Find each parasitized red blood cell.
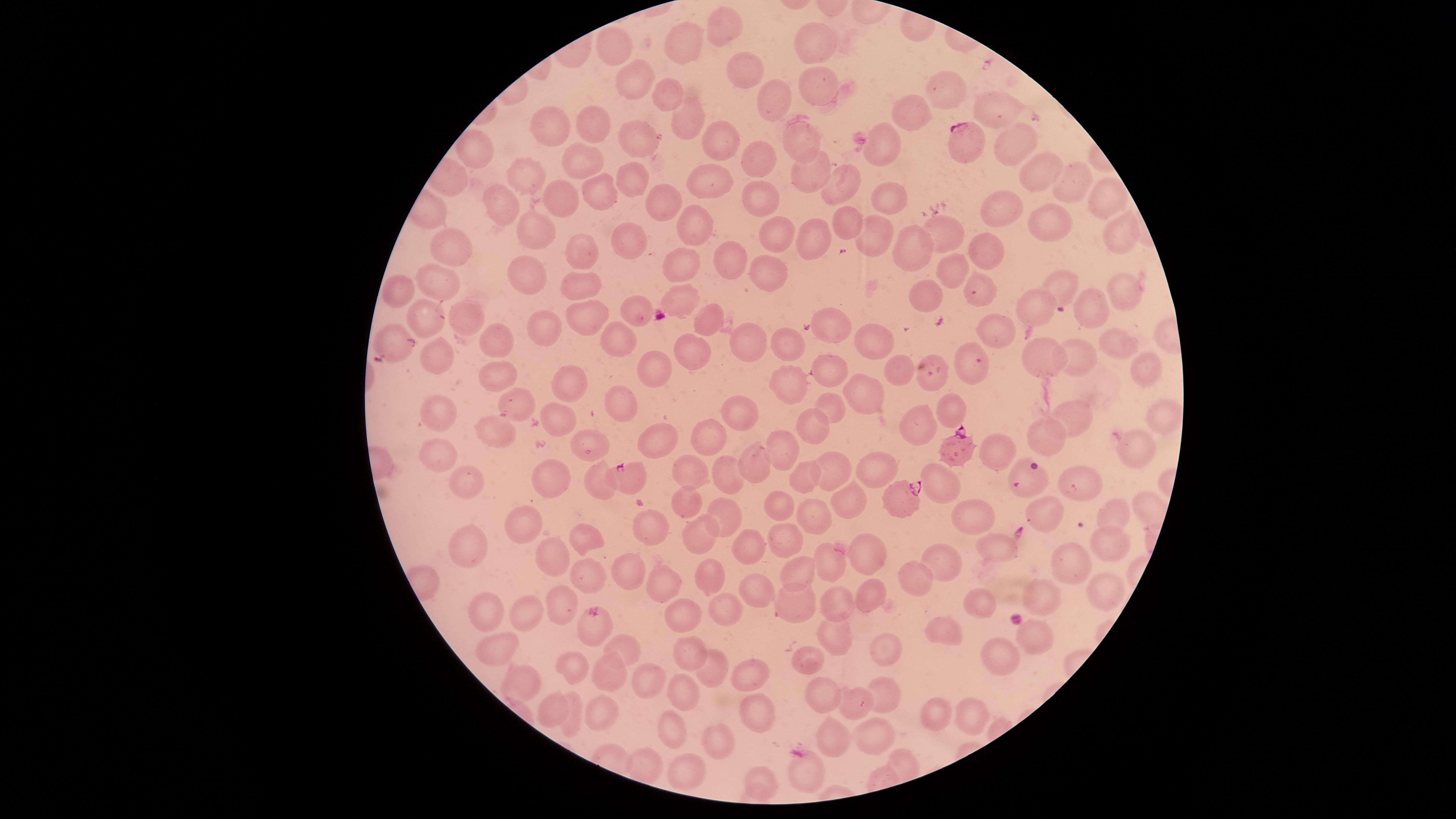
Approximate marker points, in pixels from the top-left corner.
Parasitized red blood cells: (x=967, y=145), (x=952, y=448), (x=632, y=480), (x=899, y=499).

Approximate marker points, in pixels from the top-left corner. Uninfected red blood cells: (x=723, y=23), (x=809, y=37), (x=612, y=41), (x=683, y=41), (x=743, y=71), (x=818, y=76), (x=630, y=77), (x=946, y=90), (x=669, y=91), (x=775, y=97), (x=995, y=107), (x=909, y=113), (x=684, y=120), (x=592, y=124), (x=556, y=128), (x=633, y=137), (x=719, y=138), (x=792, y=141), (x=1013, y=145), (x=888, y=148), (x=477, y=152), (x=1047, y=155), (x=763, y=159), (x=578, y=162), (x=801, y=172), (x=1035, y=172), (x=522, y=177), (x=628, y=180), (x=704, y=181), (x=840, y=184), (x=1068, y=188), (x=600, y=189), (x=1105, y=193), (x=759, y=195), (x=562, y=201), (x=889, y=201), (x=660, y=202), (x=507, y=208), (x=1000, y=213), (x=690, y=219), (x=845, y=222), (x=944, y=224), (x=1052, y=227), (x=536, y=228), (x=779, y=230), (x=807, y=234), (x=879, y=235), (x=1116, y=235), (x=628, y=241), (x=456, y=244), (x=910, y=249), (x=979, y=249), (x=585, y=251), (x=725, y=257), (x=683, y=266), (x=528, y=269), (x=957, y=271), (x=765, y=272), (x=576, y=284), (x=440, y=286), (x=401, y=287), (x=1060, y=287), (x=1113, y=291), (x=683, y=294), (x=982, y=294), (x=928, y=299), (x=1031, y=309), (x=633, y=312), (x=1093, y=312), (x=461, y=314), (x=422, y=318), (x=584, y=319), (x=704, y=324), (x=545, y=325), (x=994, y=328), (x=831, y=329), (x=497, y=334), (x=872, y=336), (x=751, y=337), (x=395, y=341), (x=620, y=342), (x=795, y=342), (x=1115, y=343), (x=442, y=352), (x=695, y=353), (x=1079, y=358), (x=1039, y=359), (x=829, y=363), (x=1145, y=366), (x=893, y=370), (x=648, y=371), (x=966, y=371), (x=498, y=377), (x=787, y=383), (x=569, y=388), (x=859, y=390), (x=516, y=398), (x=621, y=406), (x=832, y=408), (x=947, y=410), (x=738, y=414), (x=1164, y=414), (x=1073, y=416), (x=435, y=419), (x=811, y=423), (x=917, y=429), (x=659, y=432), (x=708, y=435), (x=1046, y=436), (x=504, y=439), (x=586, y=442), (x=785, y=446), (x=1133, y=447), (x=997, y=451), (x=436, y=459), (x=751, y=461), (x=828, y=467), (x=875, y=467), (x=1021, y=469), (x=693, y=471), (x=466, y=477), (x=726, y=477), (x=554, y=478), (x=801, y=480), (x=937, y=481), (x=597, y=485), (x=1074, y=486), (x=686, y=499), (x=846, y=501), (x=776, y=504), (x=729, y=509), (x=1115, y=512), (x=1046, y=513), (x=975, y=516), (x=815, y=517), (x=643, y=523), (x=524, y=526), (x=585, y=537), (x=696, y=537), (x=785, y=539), (x=747, y=544), (x=1105, y=544), (x=990, y=547), (x=461, y=551), (x=867, y=551), (x=940, y=559), (x=555, y=562), (x=832, y=562), (x=1066, y=563), (x=801, y=565), (x=628, y=572), (x=588, y=574), (x=710, y=577), (x=665, y=583), (x=918, y=583), (x=762, y=587), (x=1039, y=593), (x=1104, y=593), (x=869, y=598), (x=836, y=600), (x=794, y=601), (x=977, y=601), (x=560, y=608), (x=724, y=609), (x=512, y=611), (x=483, y=612), (x=680, y=620), (x=597, y=630), (x=943, y=633), (x=1031, y=637), (x=880, y=640), (x=836, y=644), (x=501, y=646), (x=624, y=648), (x=684, y=655), (x=1000, y=655), (x=573, y=664), (x=808, y=664), (x=710, y=668), (x=750, y=669), (x=605, y=676), (x=653, y=679), (x=518, y=686), (x=679, y=690), (x=824, y=697), (x=884, y=697), (x=856, y=701), (x=601, y=709), (x=758, y=711), (x=552, y=713), (x=972, y=713), (x=933, y=715), (x=574, y=716), (x=672, y=727), (x=834, y=734), (x=877, y=734), (x=723, y=740), (x=645, y=762), (x=805, y=774), (x=693, y=776), (x=764, y=780). Thin blood smear. Species: Plasmodium falciparum. Smartphone photograph through the microscope eyepiece. Giemsa stain. Single field of view. The visible region is circular. Image is 1456×819 pixels.